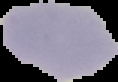
Summary:
  - Malaria status: uninfected
  - Image type: cell region segmented out of the field of view; surrounding area masked to black
  - Preparation: thin blood smear
  - Image size: 118×82 pixels